Identify the blood parasite species.
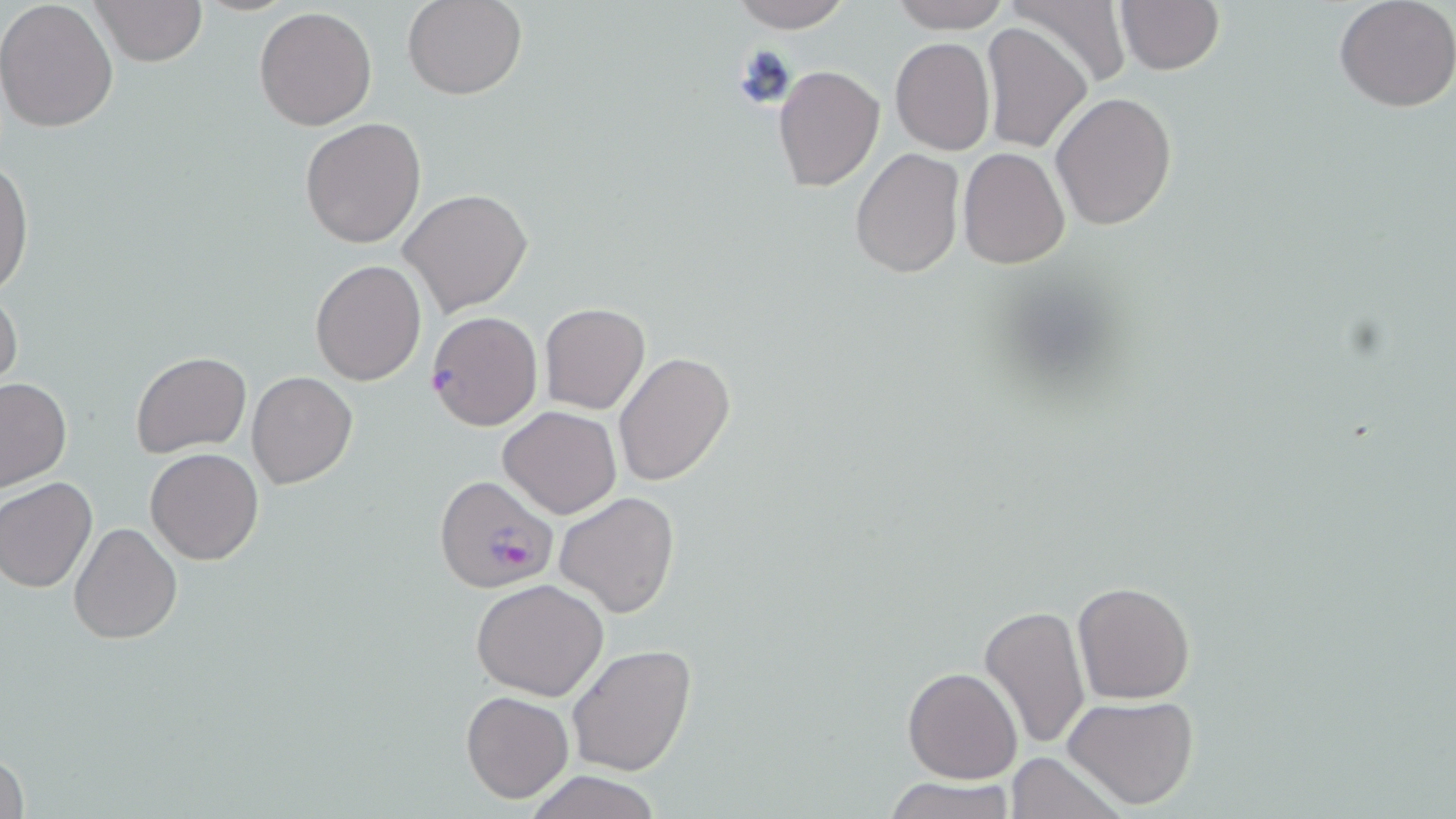
Plasmodium falciparum.

Summary:
  - Coordinate format: approximate bounding boxes as (x1,y1)-(x2,y2) corner pairs in pixels
  - Uninfected red blood cell locations: (92,0)-(208,67), (401,0)-(527,100), (726,0)-(859,28), (889,0)-(1011,32), (1002,0)-(1131,90), (1113,1)-(1224,76), (1332,1)-(1456,113), (0,2)-(120,134), (253,7)-(377,130), (981,23)-(1093,153), (892,38)-(994,155), (772,65)-(884,191), (1051,93)-(1178,230), (299,117)-(426,250), (959,146)-(1070,268), (849,148)-(963,281), (0,157)-(34,302), (398,188)-(532,315), (311,259)-(426,386), (0,283)-(23,398), (539,303)-(651,414), (613,350)-(738,488), (131,351)-(251,457), (246,372)-(358,490), (0,377)-(72,492), (498,407)-(621,519), (145,447)-(264,565), (0,477)-(97,593), (554,490)-(679,618), (68,522)-(182,644), (471,579)-(610,701), (1072,580)-(1196,703), (977,603)-(1091,750), (565,644)-(698,775), (903,666)-(1021,783), (460,690)-(574,803), (1064,695)-(1199,812), (1,744)-(28,819), (1005,753)-(1126,818), (525,770)-(662,819), (884,775)-(1017,819)
  - Plasmodium falciparum-infected red blood cell locations: (425,310)-(543,432), (437,475)-(559,595)
  - Field of view: single
  - Preparation: thin blood smear
  - Modality: optical microscopy
  - Image size: 1456×819 pixels
  - Magnification: 1000x
  - Stain: May-Grünwald-Giemsa